Find each parasitized RBC.
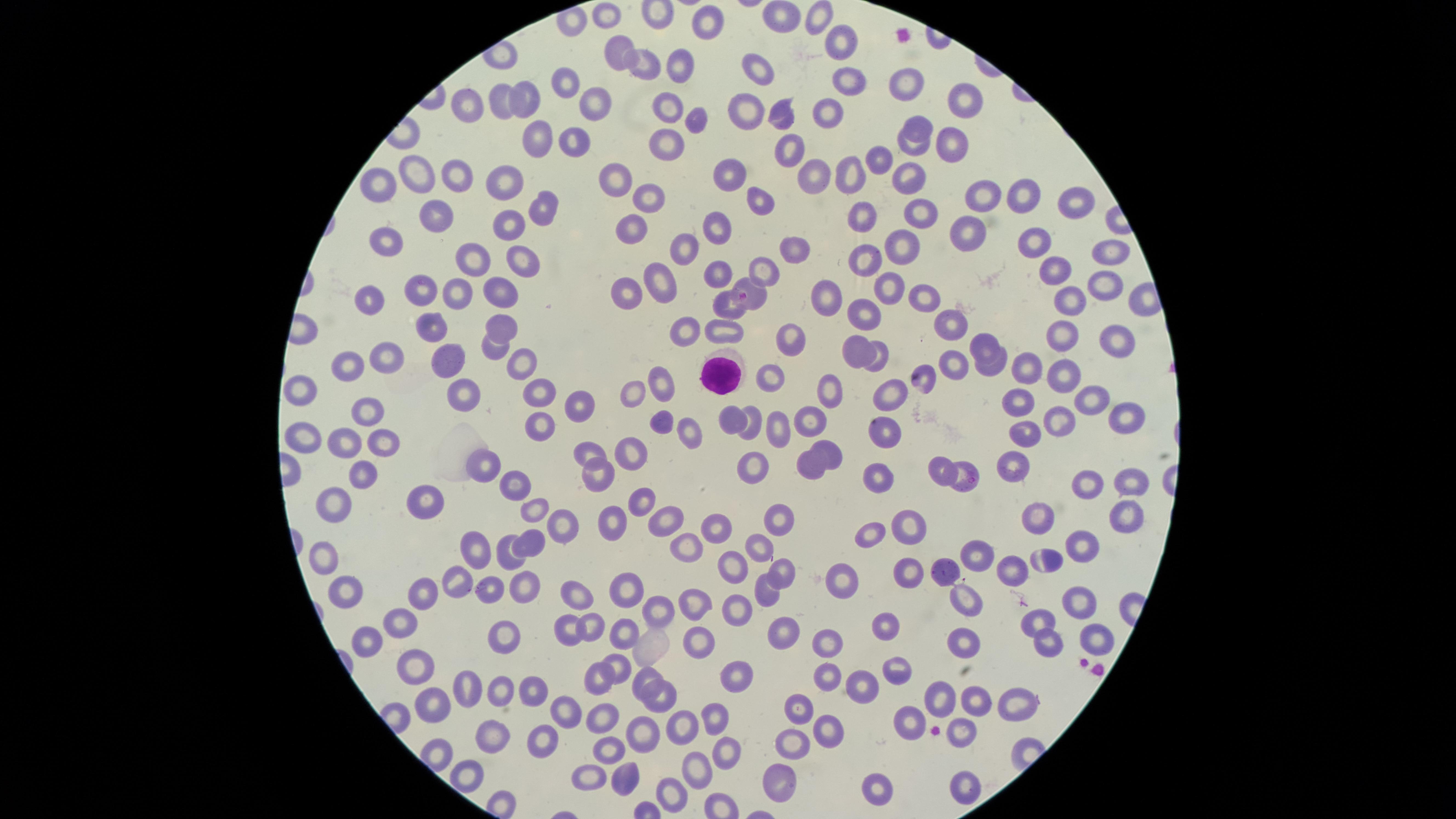
Approximate marker points as {x, y} in pixels.
Parasitized RBCs: {751, 293}.

preparation = thin blood film
image size = 1456×819 pixels
capture = smartphone photograph through the microscope eyepiece
uninfected RBCs = approximate marker points as {x, y} in pixels: {607, 13}, {781, 15}, {816, 15}, {704, 22}, {840, 40}, {621, 47}, {647, 64}, {683, 65}, {756, 65}, {849, 79}, {911, 83}, {568, 86}, {529, 95}, {963, 100}, {595, 101}, {501, 102}, {471, 104}, {668, 104}, {748, 104}, {826, 111}, {782, 112}, {691, 121}, {920, 126}, {545, 134}, {574, 137}, {953, 138}, {671, 144}, {790, 146}, {915, 148}, {878, 162}, {735, 169}, {421, 171}, {855, 171}, {455, 174}, {506, 174}, {617, 177}, {912, 177}, {812, 179}, {378, 180}, {1023, 194}, {647, 195}, {985, 195}, {1076, 195}, {760, 198}, {540, 210}, {866, 211}, {923, 213}, {439, 214}, {510, 220}, {630, 224}, {722, 224}, {966, 230}, {389, 236}, {1032, 239}, {905, 246}, {684, 247}, {1114, 247}, {791, 248}, {477, 256}, {515, 259}, {867, 261}, {760, 264}, {1050, 268}, {722, 270}, {664, 278}, {1096, 283}, {891, 285}, {427, 289}, {457, 290}, {500, 290}, {622, 292}, {920, 295}, {829, 297}, {372, 298}, {1067, 299}, {725, 303}, {866, 310}, {500, 318}, {431, 320}, {683, 325}, {950, 325}, {727, 328}, {786, 335}, {1062, 335}, {1112, 336}, {984, 341}, {496, 346}, {854, 347}, {386, 353}, {347, 360}, {443, 360}, {520, 360}, {1026, 361}, {875, 363}, {954, 365}, {990, 365}, {1057, 373}, {769, 376}, {924, 379}, {665, 381}, {828, 382}, {302, 387}, {892, 387}, {543, 392}, {463, 393}, {632, 395}, {1088, 395}, {1023, 403}, {571, 405}, {363, 409}, {752, 416}, {1127, 417}, {1062, 418}, {663, 419}, {729, 420}, {539, 423}, {809, 424}, {776, 428}, {887, 430}, {1028, 430}, {305, 434}, {692, 435}, {347, 436}, {381, 438}, {834, 449}, {587, 450}, {636, 454}, {1018, 459}, {487, 463}, {938, 466}, {363, 467}, {808, 467}, {752, 470}, {596, 474}, {966, 475}, {1089, 475}, {880, 476}, {1133, 480}, {515, 482}, {643, 496}, {427, 500}, {337, 502}, {535, 508}, {1042, 511}, {664, 513}, {1129, 514}, {780, 515}, {613, 516}, {907, 521}, {715, 522}, {567, 526}, {871, 536}, {688, 539}, {530, 540}, {760, 543}, {1082, 546}, {477, 549}, {976, 552}, {1048, 554}, {324, 560}, {509, 560}, {736, 563}, {911, 563}, {780, 565}, {1018, 566}, {949, 567}, {461, 576}, {842, 579}, {633, 583}, {523, 584}, {489, 585}, {767, 586}, {351, 590}, {420, 594}, {1079, 598}, {576, 599}, {697, 603}, {966, 604}, {665, 608}, {740, 610}, {1042, 615}, {405, 620}, {886, 622}, {591, 625}, {627, 627}, {567, 630}, {782, 630}, {1095, 634}, {368, 637}, {504, 637}, {965, 637}, {833, 640}, {697, 644}, {1044, 644}, {414, 663}, {897, 665}, {615, 667}, {829, 671}, {738, 672}, {650, 676}, {598, 679}, {863, 681}, {471, 685}, {942, 691}, {531, 692}, {498, 693}, {971, 696}, {1014, 696}, {663, 698}, {431, 704}, {804, 706}, {563, 707}, {715, 714}, {600, 719}, {914, 724}, {824, 725}, {686, 727}, {963, 731}, {644, 736}, {794, 739}, {493, 741}, {543, 744}, {611, 747}, {724, 748}, {443, 752}, {699, 763}, {470, 771}, {623, 775}, {592, 776}, {779, 776}, {965, 783}, {882, 784}, {670, 793}
WBCs = approximate marker points as {x, y} in pixels: {722, 373}
stain = Giemsa
species = Plasmodium falciparum
visible region = circular
field of view = single